Assess the morphology of the erythrocytes.
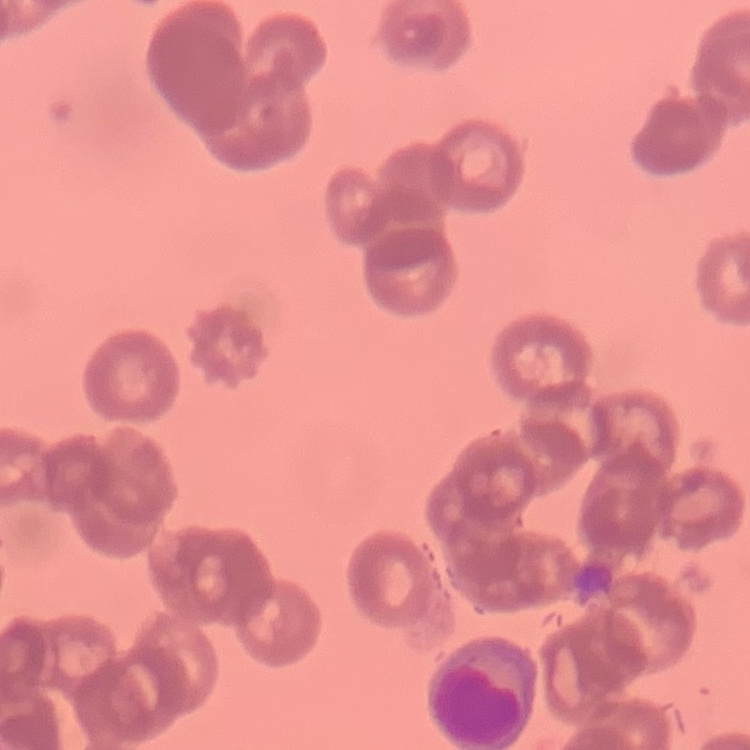

They show rouleaux formation.

Field's or Giemsa stain. One tile cut from a larger photomicrograph. Thin blood smear.